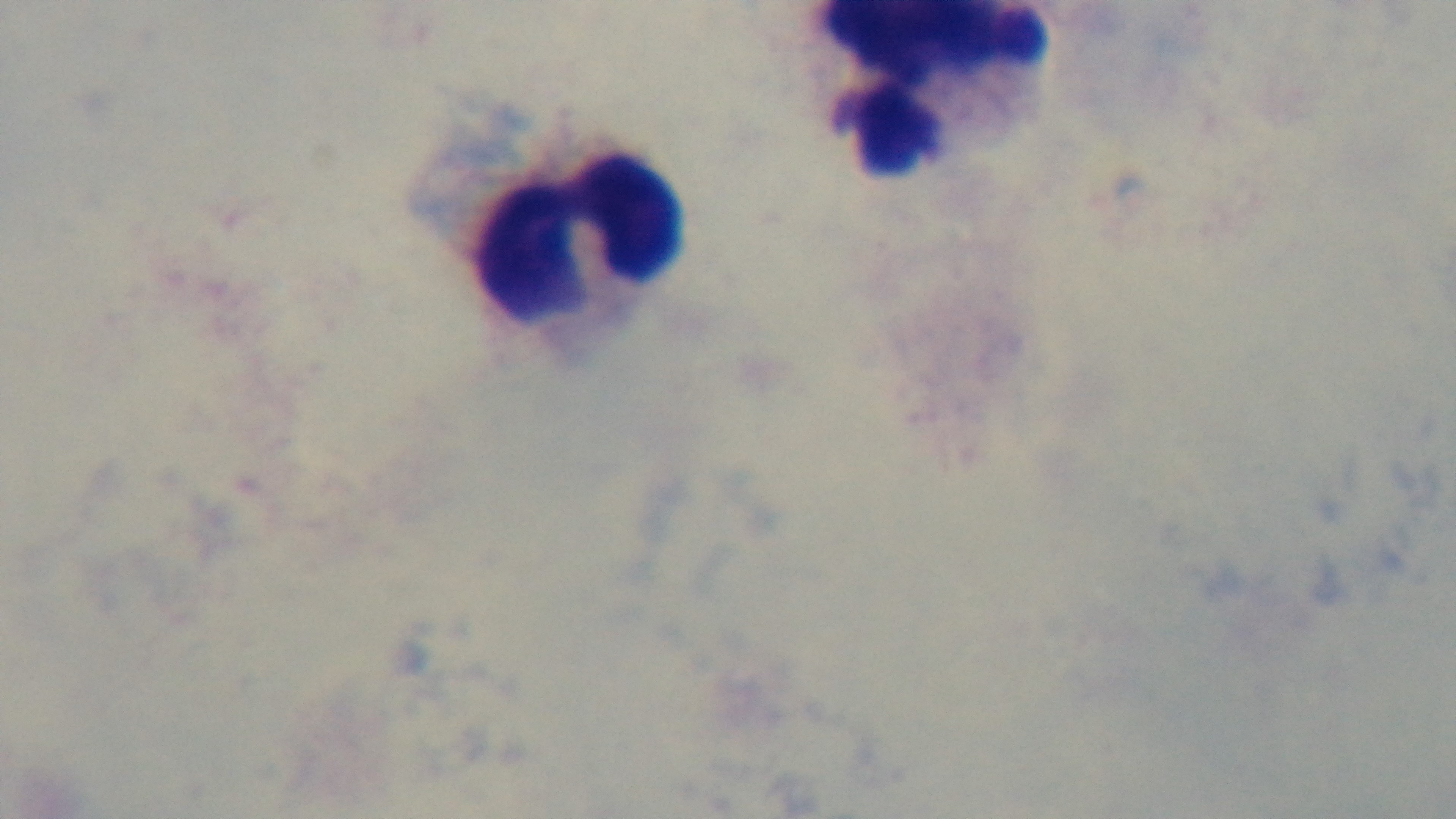
capture: mounted 4K digital camera
preparation: thick smear
modality: light microscopy
field_of_view: one from the slide
malaria_status: uninfected
stain: Giemsa
objective: 100x oil immersion